Comment on the morphology of the erythrocytes.
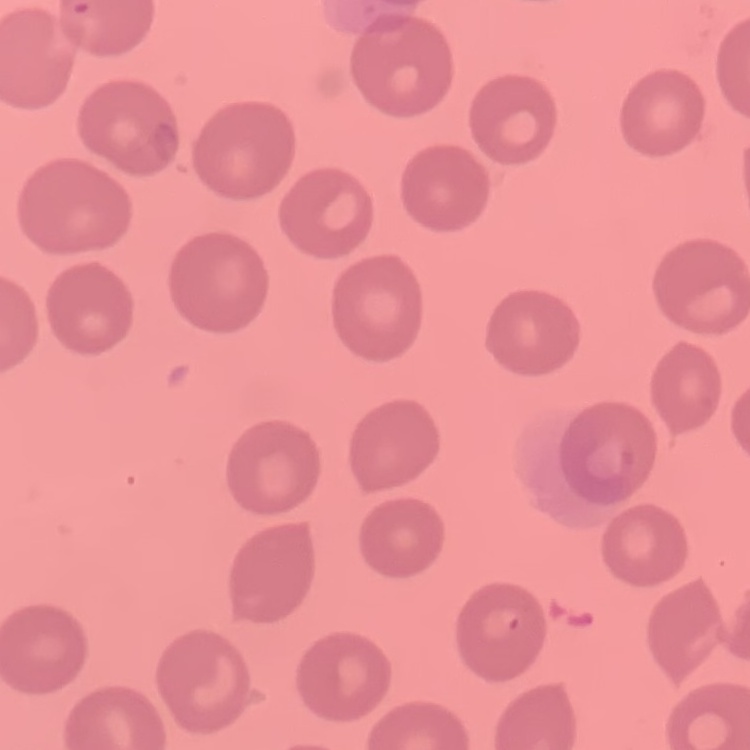

They show no rouleaux formation.

Summary:
  - Image type: one tile cut from a larger photomicrograph
  - Stain: Field's or Giemsa
  - Preparation: thin peripheral smear